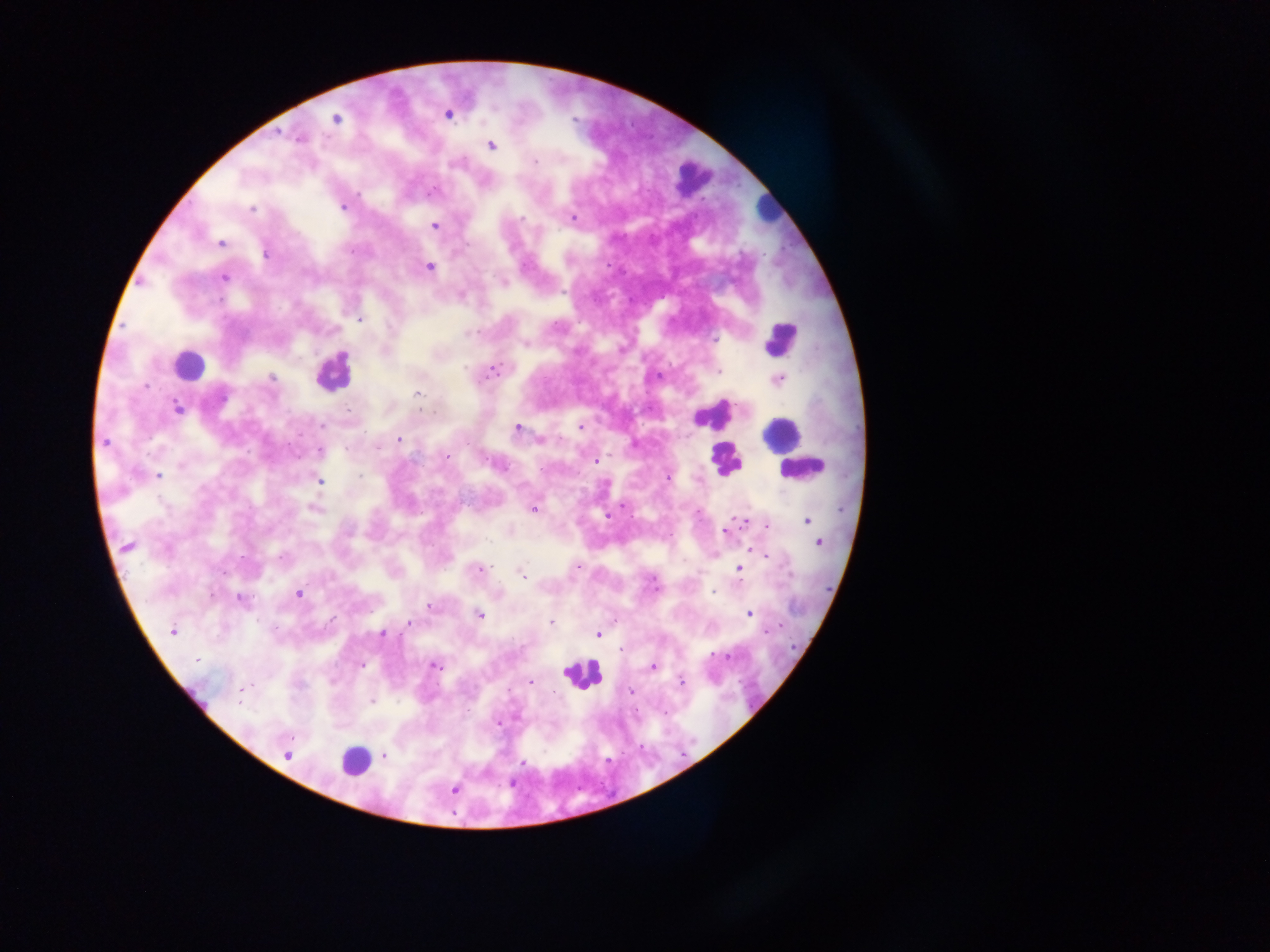 Approximate centers as {x, y} in pixels. Plasmodium parasite locations: {449, 116}, {336, 119}, {492, 146}, {534, 162}, {432, 190}, {357, 195}, {343, 207}, {252, 209}, {524, 218}, {573, 218}, {435, 225}, {220, 242}, {265, 255}, {430, 266}, {226, 277}, {503, 280}, {143, 286}, {359, 319}, {468, 334}, {717, 337}, {525, 344}, {620, 345}, {347, 353}, {465, 368}, {492, 370}, {720, 370}, {659, 376}, {272, 377}, {778, 377}, {146, 385}, {417, 394}, {179, 408}, {421, 410}, {697, 420}, {320, 425}, {582, 425}, {516, 427}, {400, 439}, {539, 439}, {104, 441}, {632, 443}, {447, 456}, {596, 462}, {182, 464}, {498, 466}, {158, 475}, {668, 478}, {321, 480}, {621, 506}, {313, 507}, {534, 510}, {604, 515}, {804, 520}, {770, 523}, {733, 528}, {818, 544}, {127, 547}, {751, 549}, {758, 551}, {717, 553}, {573, 565}, {739, 568}, {479, 569}, {521, 572}, {712, 592}, {296, 593}, {240, 599}, {429, 606}, {750, 614}, {480, 615}, {550, 622}, {407, 623}, {171, 630}, {383, 633}, {598, 634}, {621, 648}, {724, 654}, {195, 661}, {434, 665}, {360, 666}, {653, 666}, {532, 681}, {681, 681}, {330, 682}, {630, 694}, {371, 701}, {240, 703}, {496, 724}, {289, 756}, {523, 763}, {511, 781}, {453, 789}. Leukocyte locations: {691, 186}, {767, 207}, {781, 334}, {185, 360}, {326, 374}, {719, 411}, {723, 462}, {803, 472}, {581, 676}, {355, 757}. Image is 1270×952 pixels. Photographed through a microscope with a mobile-phone camera. One field of view. Thick blood smear. Sample from Ghana.